Assess the morphology of the erythrocytes.
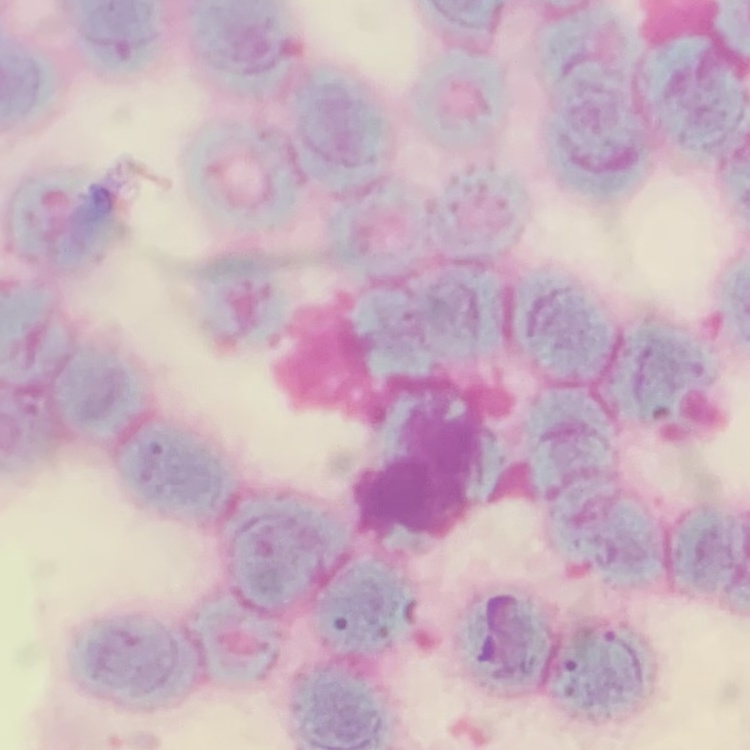
Rouleaux formation.

Thin peripheral smear. Square crop of a larger photomicrograph. Field's or Giemsa stain.